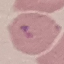
Summary:
  - Result: no malaria parasites seen
  - Capture: smartphone through the microscope eyepiece
  - Stain: Giemsa
  - Preparation: thin blood film
  - Image type: cell patch, automatically extracted from a larger field of view and resized to 64 × 64 pixels